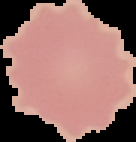

image type = segmented cell region with the area outside set to black
result = negative for Plasmodium parasites
image size = 136×142 pixels
preparation = thin blood film